Give the extent of all Plasmodium vivax-infected red blood cells.
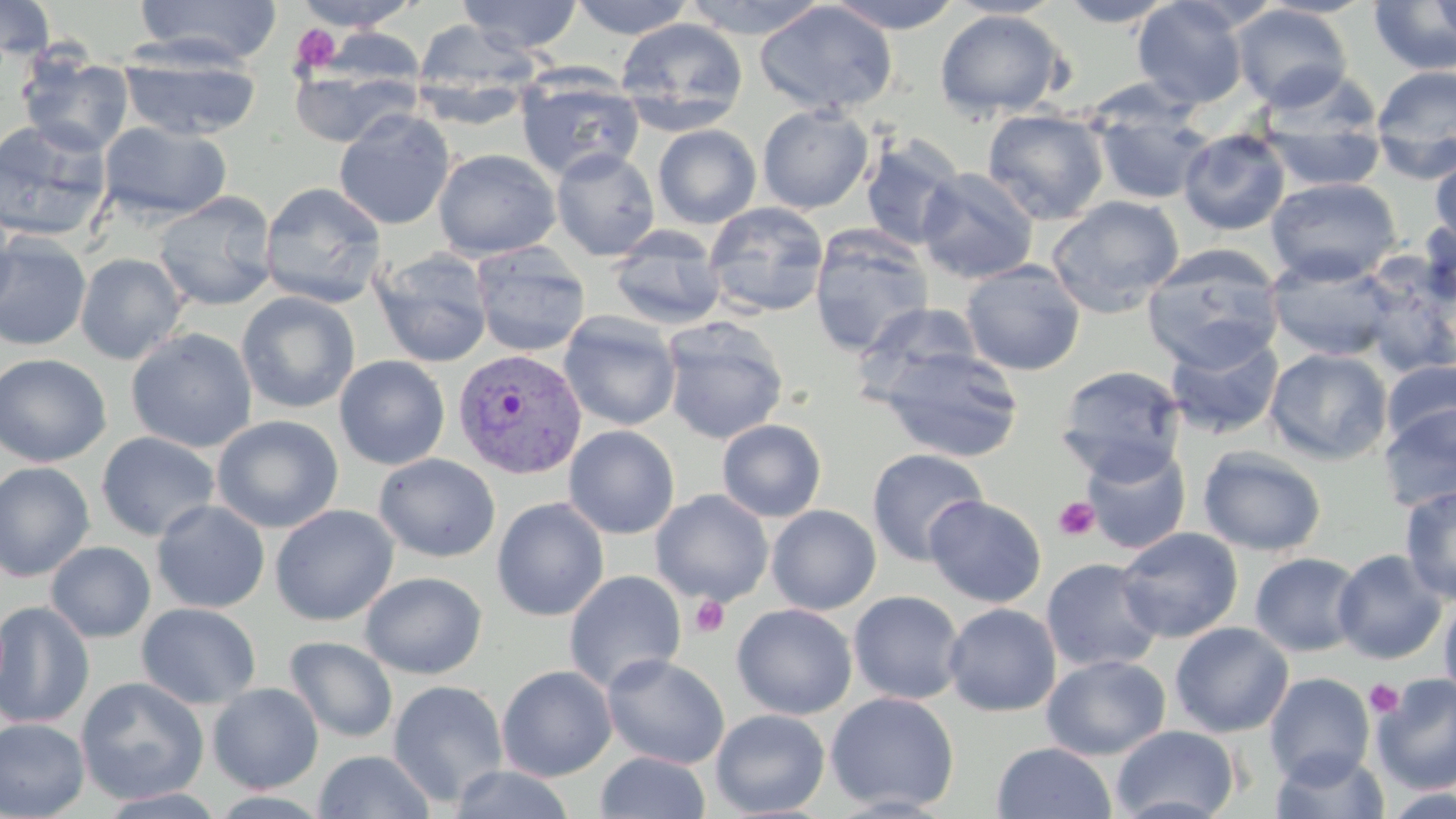

Approximate bounding boxes as [x1, y1, x2, y2] in pixels.
Plasmodium vivax-infected red blood cells: [453, 348, 587, 480].

Summary:
  - Platelet locations: [289, 23, 342, 76], [1054, 496, 1101, 541], [690, 596, 729, 639], [1364, 679, 1404, 718]
  - Uninfected red blood cell locations: [0, 0, 56, 61], [132, 0, 283, 67], [289, 0, 423, 32], [457, 0, 583, 53], [567, 0, 697, 39], [680, 0, 832, 39], [824, 0, 965, 34], [945, 0, 1066, 19], [1257, 0, 1379, 19], [1057, 1, 1178, 28], [1132, 1, 1249, 109], [1368, 1, 1456, 75], [1430, 1, 1456, 41], [755, 2, 899, 116], [1232, 4, 1353, 111], [934, 10, 1068, 120], [616, 18, 749, 136], [411, 19, 541, 121], [314, 28, 429, 92], [119, 49, 261, 141], [18, 52, 134, 158], [288, 62, 422, 148], [1370, 65, 1456, 181], [515, 68, 645, 181], [1092, 101, 1215, 206], [757, 104, 873, 214], [982, 108, 1110, 225], [334, 109, 455, 231], [0, 118, 114, 243], [98, 121, 231, 222], [1260, 121, 1387, 192], [652, 124, 761, 229], [1178, 128, 1291, 235], [860, 136, 965, 251], [433, 148, 561, 260], [551, 148, 660, 261], [1430, 154, 1456, 249], [916, 167, 1039, 285], [1265, 176, 1401, 285], [259, 182, 387, 308], [153, 190, 278, 311], [1045, 196, 1184, 318], [0, 200, 20, 319], [703, 202, 830, 319], [1419, 216, 1456, 309], [809, 225, 934, 357], [607, 226, 728, 331], [0, 235, 92, 351], [469, 243, 591, 357], [1142, 245, 1285, 371], [371, 249, 494, 368], [75, 253, 188, 365], [1266, 253, 1400, 363], [1354, 259, 1455, 378], [960, 261, 1086, 376], [236, 292, 360, 414], [853, 302, 984, 406], [558, 311, 682, 431], [660, 318, 788, 444], [126, 328, 258, 453], [1164, 330, 1284, 439], [878, 347, 1025, 464], [1265, 348, 1393, 465], [0, 353, 112, 467], [334, 355, 450, 470], [1381, 360, 1456, 449], [1055, 365, 1185, 481], [1377, 402, 1456, 514], [211, 415, 344, 534], [716, 419, 827, 522], [564, 425, 680, 539], [96, 431, 221, 542], [1081, 443, 1192, 555], [1197, 446, 1327, 557], [866, 448, 990, 567], [373, 453, 501, 563], [0, 461, 95, 581], [1399, 484, 1456, 604], [650, 489, 773, 606], [925, 495, 1047, 608], [491, 498, 609, 621], [151, 500, 270, 613], [269, 505, 399, 626], [766, 505, 881, 615], [1115, 527, 1243, 643], [45, 541, 156, 643], [1332, 549, 1448, 664], [1250, 552, 1363, 656], [1040, 557, 1165, 673], [564, 570, 687, 695], [359, 572, 487, 679], [848, 590, 966, 704], [1439, 590, 1456, 708], [0, 601, 95, 728], [136, 602, 261, 710], [731, 603, 858, 720], [943, 603, 1062, 717], [1170, 622, 1294, 737], [284, 636, 398, 743], [602, 654, 730, 769], [1041, 654, 1170, 760], [496, 665, 617, 781], [1264, 672, 1375, 785], [1371, 673, 1456, 794], [75, 676, 210, 805], [387, 679, 510, 807], [207, 682, 324, 793], [825, 692, 960, 812], [710, 709, 830, 817], [0, 718, 91, 819], [1110, 724, 1240, 819], [991, 741, 1117, 819], [1271, 748, 1390, 819], [313, 750, 436, 819], [595, 751, 711, 819], [448, 765, 578, 819], [1380, 787, 1456, 819], [96, 788, 228, 818]
  - Slide-level diagnosis: Plasmodium vivax
  - Field of view: single
  - Magnification: 1000x
  - Image size: 1456×819 pixels
  - Modality: optical microscopy
  - Stain: May-Grünwald-Giemsa
  - Preparation: thin blood film